Classify this cell by malaria status.
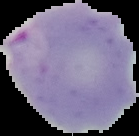
Parasitized.

preparation = thin blood film
image type = segmented cell region with the area outside set to black
image size = 139×136 pixels